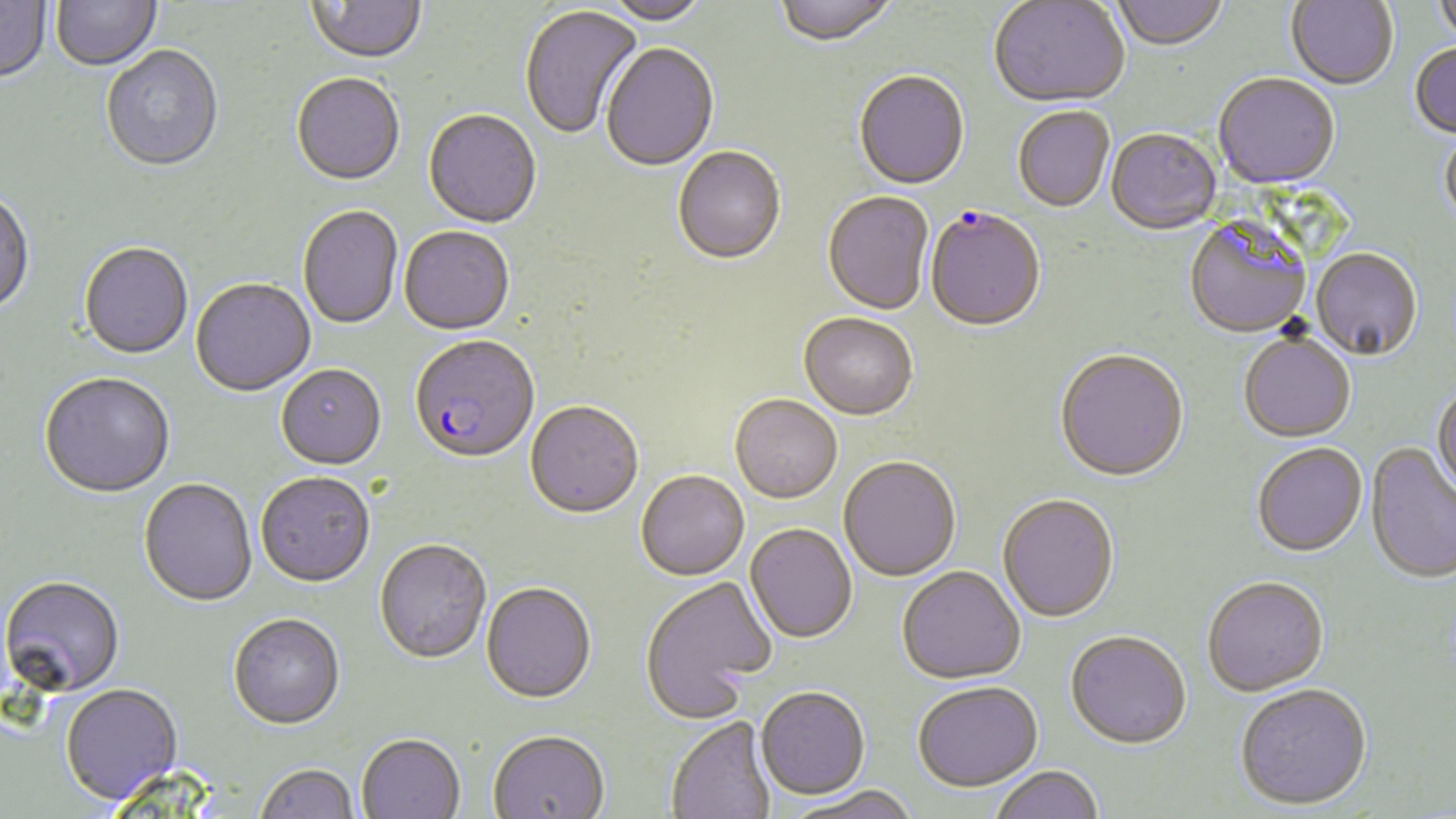 Approximate bounding boxes as (x1, y1, x2, y2) in pixels. Uninfected red blood cell locations: (0, 0, 52, 86), (52, 0, 162, 73), (307, 0, 427, 68), (775, 0, 898, 49), (1111, 0, 1229, 53), (1286, 0, 1398, 91), (1434, 0, 1456, 48), (597, 1, 711, 28), (989, 1, 1130, 110), (519, 5, 645, 141), (601, 45, 719, 173), (1409, 45, 1456, 140), (101, 47, 224, 175), (853, 73, 970, 192), (291, 75, 405, 188), (1213, 76, 1340, 191), (1013, 108, 1114, 214), (423, 111, 542, 230), (1439, 129, 1456, 231), (1106, 131, 1221, 237), (672, 148, 786, 267), (0, 192, 35, 317), (823, 193, 934, 317), (298, 207, 403, 330), (1185, 222, 1311, 340), (399, 228, 515, 337), (79, 244, 193, 361), (1311, 250, 1422, 363), (190, 279, 316, 399), (798, 315, 918, 422), (1239, 335, 1356, 444), (1055, 352, 1189, 484), (276, 367, 387, 472), (39, 374, 175, 501), (1431, 386, 1456, 500), (730, 397, 842, 505), (525, 403, 644, 521), (1365, 444, 1456, 586), (1253, 445, 1368, 559), (838, 458, 961, 582), (636, 473, 749, 582), (256, 474, 375, 590), (138, 480, 257, 609), (998, 496, 1120, 624), (745, 524, 857, 645), (374, 541, 491, 666), (897, 568, 1025, 686), (640, 577, 775, 722), (0, 578, 124, 700), (1202, 579, 1329, 699), (481, 584, 597, 706), (228, 616, 345, 732), (1065, 634, 1191, 752), (913, 684, 1043, 796), (60, 686, 183, 807), (1235, 687, 1373, 813), (756, 689, 869, 802), (666, 718, 776, 819), (488, 733, 609, 819), (357, 736, 465, 819), (254, 765, 360, 819), (991, 768, 1104, 819), (790, 788, 921, 819). Plasmodium falciparum-infected red blood cell locations: (925, 210, 1046, 334), (409, 338, 540, 466). Slide-level diagnosis: Plasmodium falciparum. Thin blood film. Captured at 1000x magnification. Optical microscopy. Image is 1456×819 pixels. May-Grünwald-Giemsa stain. One field of a larger specimen.